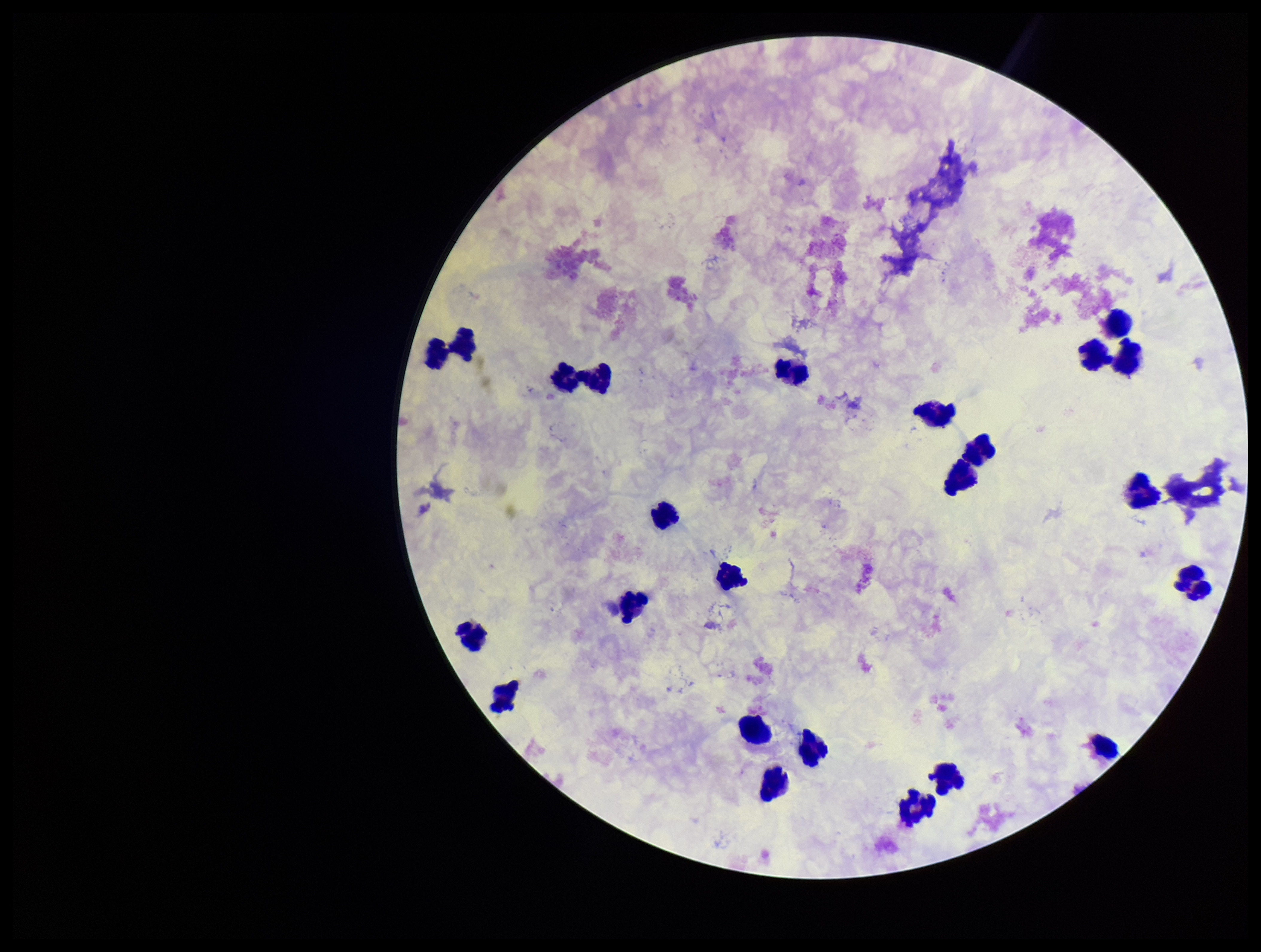

Preparation: thick smear. Image is 1261×952 pixels. One field from this slide. Patient malaria status: negative. Plasmodium parasites: none identified. Photographed through the microscope eyepiece with a smartphone camera. Stained with Giemsa. Parasite count: 0. Leukocyte count: 23.